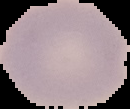 Result: no Plasmodium parasites seen. The area outside the segmented cell region is set to black. Image is 130×109 pixels. From a thin blood film.